Locate and identify every blood parasite.
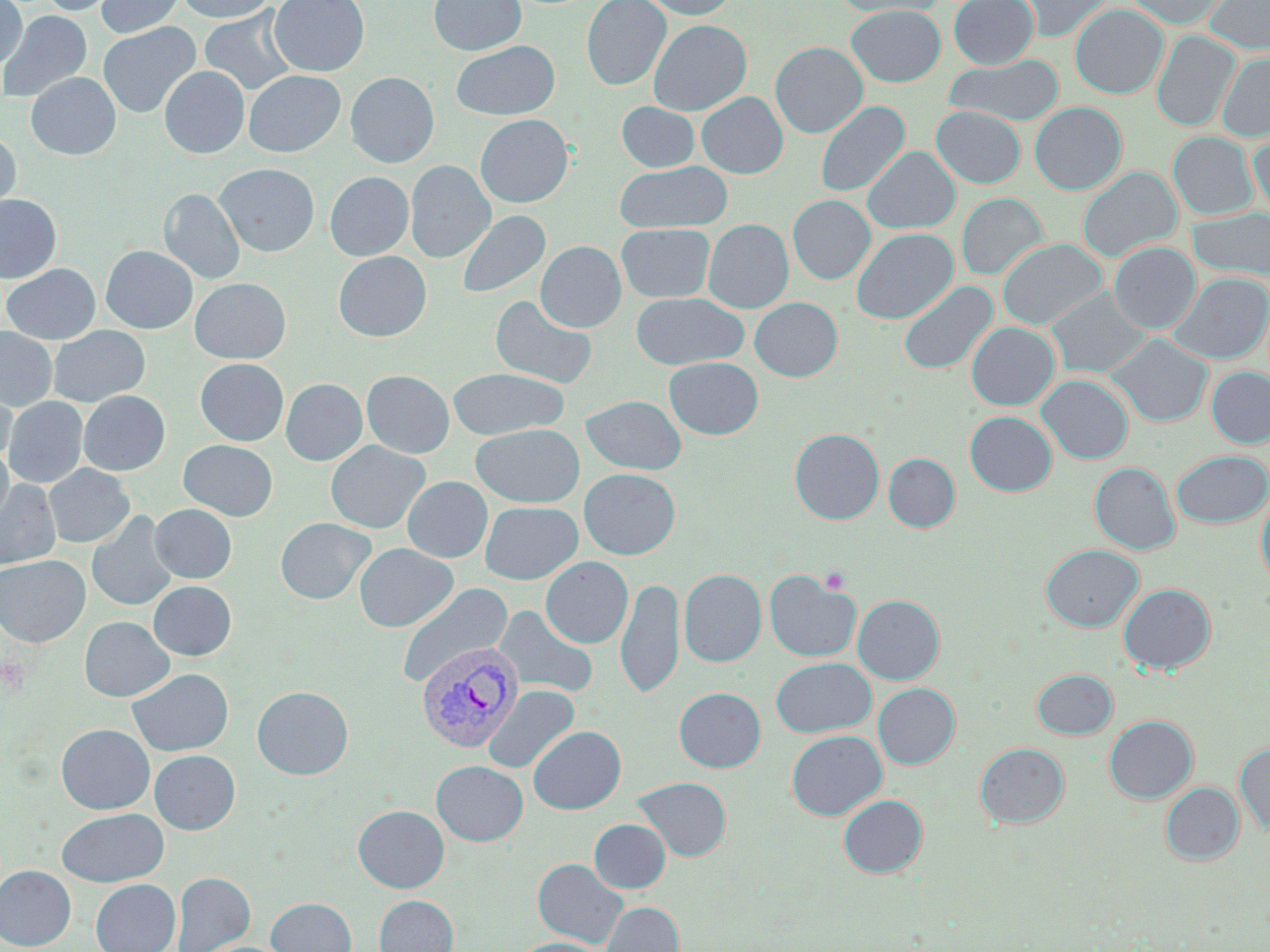
Approximate bounding boxes as named x1/y1/x2/y2 corners in pixels.
Plasmodium vivax-infected red blood cells: (x1=416, y1=640, x2=523, y2=752).
No Plasmodium falciparum, Plasmodium ovale, Plasmodium malariae, Babesia divergens, or Trypanosoma brucei observed.

{
  "slide_level_diagnosis": "Plasmodium vivax",
  "modality": "light microscopy",
  "platelet_locations": "approximate bounding boxes as named x1/y1/x2/y2 corners in pixels: (x1=821, y1=567, x2=851, y2=595), (x1=1, y1=656, x2=31, y2=698)",
  "field_of_view": "one of a larger specimen",
  "preparation": "thin blood film",
  "uninfected_red_blood_cell_locations": "approximate bounding boxes as named x1/y1/x2/y2 corners in pixels: (x1=0, y1=0, x2=27, y2=70), (x1=37, y1=0, x2=119, y2=16), (x1=96, y1=0, x2=185, y2=37), (x1=176, y1=0, x2=276, y2=23), (x1=268, y1=0, x2=370, y2=77), (x1=428, y1=0, x2=526, y2=56), (x1=582, y1=0, x2=670, y2=90), (x1=640, y1=0, x2=738, y2=19), (x1=832, y1=0, x2=945, y2=18), (x1=948, y1=0, x2=1038, y2=69), (x1=1013, y1=0, x2=1112, y2=42), (x1=1125, y1=0, x2=1231, y2=28), (x1=1205, y1=0, x2=1270, y2=54), (x1=1070, y1=4, x2=1168, y2=98), (x1=846, y1=5, x2=946, y2=86), (x1=199, y1=7, x2=298, y2=96), (x1=0, y1=10, x2=92, y2=104), (x1=648, y1=19, x2=752, y2=115), (x1=97, y1=22, x2=201, y2=119), (x1=1152, y1=30, x2=1240, y2=132), (x1=452, y1=40, x2=559, y2=120), (x1=770, y1=41, x2=868, y2=138), (x1=1217, y1=52, x2=1270, y2=141), (x1=946, y1=54, x2=1063, y2=128), (x1=159, y1=66, x2=250, y2=159), (x1=243, y1=70, x2=345, y2=157), (x1=26, y1=72, x2=120, y2=160), (x1=345, y1=72, x2=439, y2=168), (x1=696, y1=92, x2=788, y2=178), (x1=815, y1=101, x2=910, y2=197), (x1=617, y1=102, x2=700, y2=172), (x1=1029, y1=102, x2=1126, y2=194), (x1=932, y1=106, x2=1025, y2=188), (x1=475, y1=114, x2=573, y2=208), (x1=1249, y1=129, x2=1270, y2=219), (x1=0, y1=131, x2=21, y2=219), (x1=1169, y1=132, x2=1257, y2=220), (x1=863, y1=147, x2=960, y2=234), (x1=406, y1=160, x2=495, y2=262), (x1=614, y1=161, x2=732, y2=232), (x1=214, y1=163, x2=319, y2=256), (x1=1077, y1=166, x2=1182, y2=262), (x1=325, y1=172, x2=414, y2=260), (x1=159, y1=188, x2=245, y2=284), (x1=956, y1=193, x2=1048, y2=280), (x1=0, y1=195, x2=62, y2=282), (x1=788, y1=195, x2=875, y2=284), (x1=1188, y1=207, x2=1270, y2=280), (x1=456, y1=210, x2=550, y2=299), (x1=703, y1=219, x2=794, y2=313), (x1=616, y1=223, x2=715, y2=302), (x1=851, y1=228, x2=958, y2=324), (x1=998, y1=238, x2=1106, y2=329), (x1=536, y1=241, x2=626, y2=332), (x1=1108, y1=242, x2=1200, y2=334), (x1=100, y1=245, x2=197, y2=333), (x1=333, y1=251, x2=431, y2=342), (x1=2, y1=264, x2=100, y2=344), (x1=1170, y1=273, x2=1270, y2=364), (x1=189, y1=277, x2=291, y2=364), (x1=899, y1=281, x2=998, y2=375), (x1=1045, y1=287, x2=1152, y2=378), (x1=631, y1=292, x2=748, y2=370), (x1=490, y1=294, x2=598, y2=390), (x1=750, y1=297, x2=843, y2=381), (x1=966, y1=322, x2=1059, y2=410), (x1=48, y1=325, x2=150, y2=407), (x1=0, y1=327, x2=57, y2=411), (x1=1106, y1=333, x2=1212, y2=427), (x1=664, y1=357, x2=763, y2=439), (x1=195, y1=358, x2=289, y2=445), (x1=1206, y1=367, x2=1270, y2=447), (x1=447, y1=368, x2=569, y2=440), (x1=361, y1=370, x2=454, y2=458), (x1=1037, y1=374, x2=1133, y2=465), (x1=281, y1=378, x2=367, y2=465), (x1=0, y1=383, x2=16, y2=467), (x1=78, y1=390, x2=170, y2=475), (x1=581, y1=395, x2=686, y2=475), (x1=3, y1=396, x2=88, y2=488), (x1=964, y1=411, x2=1057, y2=496), (x1=470, y1=423, x2=584, y2=507), (x1=789, y1=428, x2=884, y2=525), (x1=178, y1=440, x2=278, y2=520), (x1=325, y1=441, x2=430, y2=534), (x1=0, y1=444, x2=13, y2=527), (x1=1171, y1=450, x2=1270, y2=528), (x1=883, y1=453, x2=960, y2=532), (x1=1090, y1=462, x2=1180, y2=555), (x1=44, y1=464, x2=134, y2=548), (x1=579, y1=469, x2=680, y2=559), (x1=403, y1=476, x2=493, y2=562), (x1=0, y1=479, x2=61, y2=569), (x1=1256, y1=490, x2=1270, y2=589), (x1=479, y1=501, x2=583, y2=584), (x1=150, y1=504, x2=236, y2=583), (x1=87, y1=511, x2=178, y2=612), (x1=275, y1=517, x2=375, y2=605), (x1=354, y1=543, x2=457, y2=632), (x1=1041, y1=544, x2=1143, y2=631), (x1=0, y1=555, x2=89, y2=647), (x1=540, y1=557, x2=633, y2=648), (x1=679, y1=569, x2=766, y2=667), (x1=764, y1=569, x2=860, y2=662), (x1=616, y1=577, x2=684, y2=698), (x1=148, y1=581, x2=236, y2=660), (x1=396, y1=583, x2=513, y2=688), (x1=1119, y1=583, x2=1216, y2=674), (x1=853, y1=594, x2=944, y2=684), (x1=492, y1=604, x2=599, y2=699), (x1=79, y1=616, x2=174, y2=701), (x1=771, y1=657, x2=876, y2=737), (x1=127, y1=668, x2=233, y2=756), (x1=1032, y1=669, x2=1117, y2=739), (x1=873, y1=683, x2=959, y2=769), (x1=251, y1=685, x2=354, y2=780), (x1=483, y1=685, x2=579, y2=775), (x1=674, y1=687, x2=765, y2=772), (x1=1104, y1=715, x2=1198, y2=803), (x1=56, y1=724, x2=154, y2=814), (x1=528, y1=725, x2=626, y2=814), (x1=786, y1=730, x2=887, y2=820), (x1=975, y1=743, x2=1069, y2=828), (x1=1235, y1=743, x2=1270, y2=836), (x1=149, y1=750, x2=240, y2=834), (x1=431, y1=760, x2=528, y2=846), (x1=632, y1=776, x2=732, y2=861), (x1=1161, y1=782, x2=1244, y2=865), (x1=838, y1=794, x2=927, y2=878), (x1=353, y1=805, x2=449, y2=892), (x1=56, y1=808, x2=168, y2=886), (x1=589, y1=819, x2=670, y2=892), (x1=532, y1=858, x2=629, y2=949), (x1=0, y1=865, x2=76, y2=949), (x1=172, y1=872, x2=255, y2=952), (x1=91, y1=879, x2=180, y2=952), (x1=374, y1=895, x2=458, y2=952), (x1=266, y1=897, x2=357, y2=952), (x1=600, y1=901, x2=684, y2=952), (x1=513, y1=937, x2=608, y2=952)",
  "magnification": "1000x",
  "stain": "May-Grünwald-Giemsa",
  "image_size": "1270×952 pixels"
}